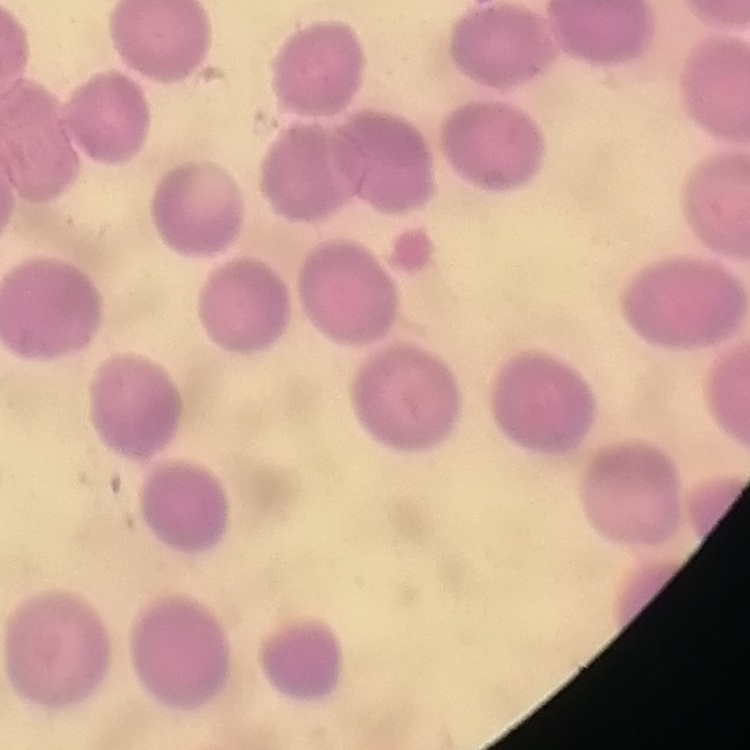

The erythrocytes show no rouleaux formation. Field's or Giemsa stain. Square crop of a larger photomicrograph. Thin peripheral smear.